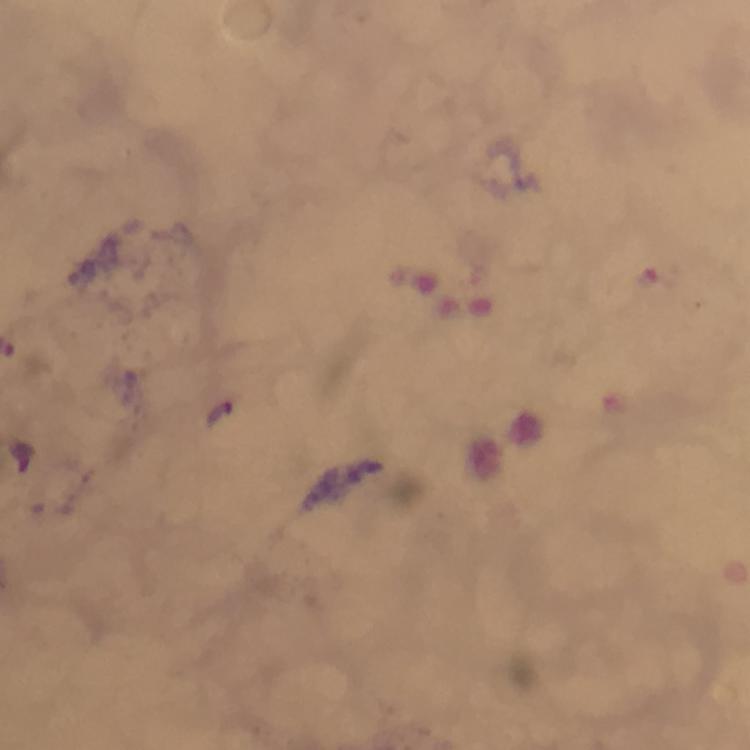

Approximate centers as [x, y] in pixels. Plasmodium parasite locations: [649, 278], [24, 457]. At 100x magnification. Immersion oil applied. Cropped region of a single field of view. Photographed through the microscope with a smartphone camera. Thick blood smear. Image is 750×750 pixels. Giemsa stain. From a malaria diagnostic workup.